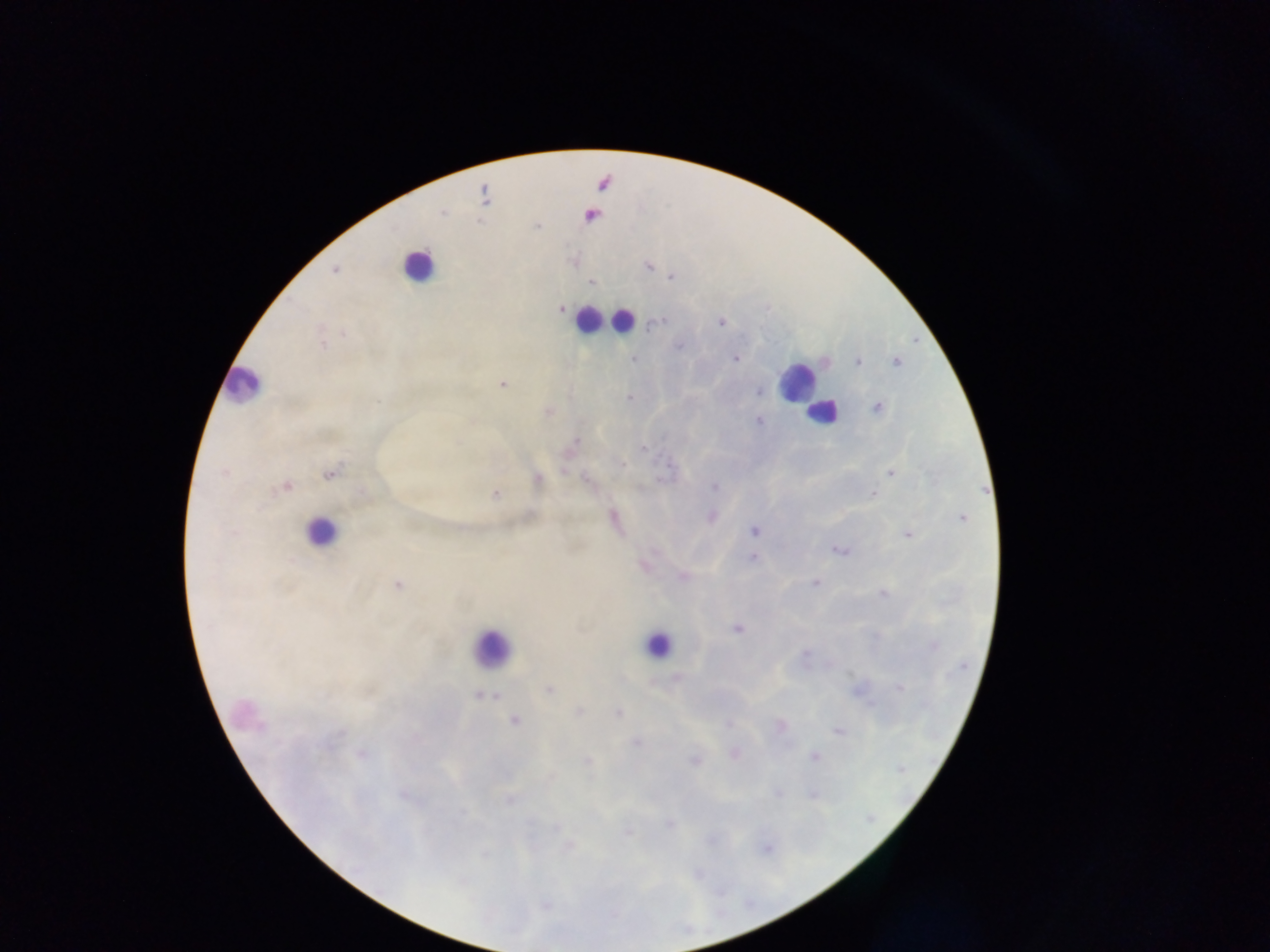 Approximate centers as [x, y] in pixels. Leukocyte locations: [417, 265], [587, 319], [623, 320], [796, 382], [244, 386], [823, 412], [321, 532], [657, 645], [491, 649]. Malaria parasite locations: [484, 196], [590, 215], [573, 262], [647, 265], [334, 269], [671, 276], [590, 282], [560, 309], [720, 322], [659, 323], [344, 334], [322, 344], [679, 345], [734, 358], [633, 359], [857, 361], [895, 362], [503, 384], [758, 392], [630, 398], [877, 407], [549, 411], [758, 420], [642, 447], [564, 470], [224, 472], [891, 472], [329, 473], [536, 480], [285, 485], [715, 487], [495, 494], [873, 495], [710, 516], [963, 518], [614, 520], [755, 530], [908, 534], [839, 550], [754, 557], [644, 565], [682, 576], [814, 582], [398, 584], [883, 593], [737, 628], [932, 645], [676, 678], [900, 688], [550, 690], [481, 694], [578, 711], [617, 712], [514, 720], [726, 724], [780, 725], [840, 732], [636, 741], [362, 754], [735, 754], [813, 756], [694, 759], [778, 791], [814, 795], [509, 799], [670, 822], [627, 831], [567, 846]. Single field of view. Photographed through a microscope with a mobile-phone camera. Image is 1270×952 pixels. Thick blood smear. Collected in Ghana.